Report the malaria status of this cell.
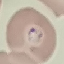

It is parasitized.

preparation: thin blood film
stain: Giemsa
capture: smartphone camera at the microscope eyepiece
image_type: automatically extracted cell patch, resized to 64 × 64 pixels